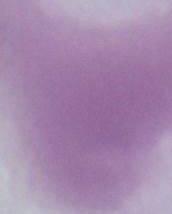 An erythrocyte is shown. Captured at 1000x magnification. Micrograph.